Classify this cell by malaria status.
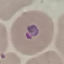
Parasitized.

Summary:
  - Stain: Giemsa
  - Preparation: thin smear
  - Image type: cell patch, automatically extracted from a larger field of view and resized to 64 × 64 pixels
  - Capture: smartphone camera at the microscope eyepiece